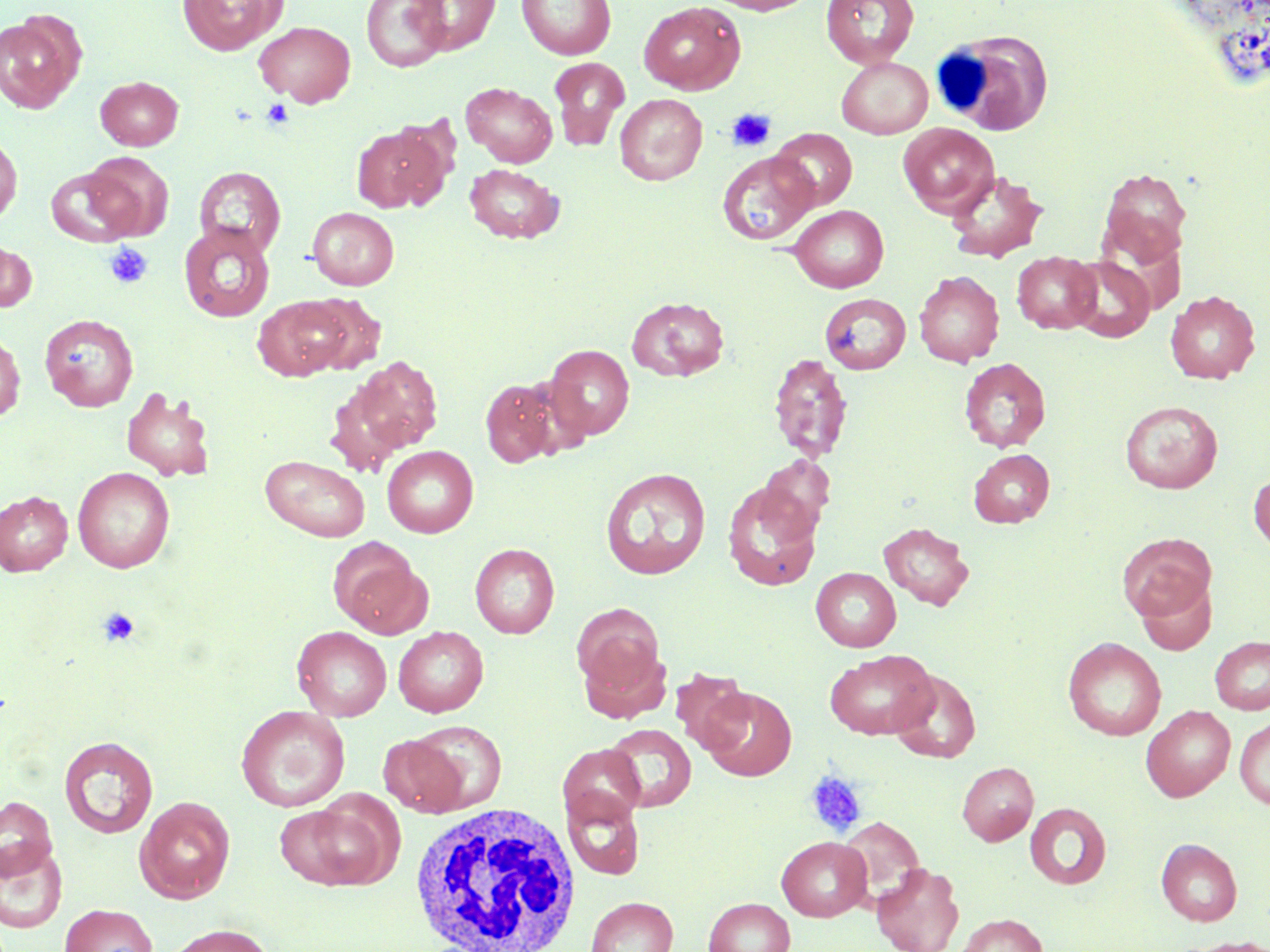 Approximate bounding boxes as [x1, y1, x2, y2] in pixels. Uninfected red blood cell locations: [177, 0, 286, 55], [361, 0, 451, 72], [408, 0, 501, 54], [517, 0, 616, 60], [705, 0, 817, 15], [821, 0, 919, 69], [639, 1, 745, 94], [0, 12, 84, 114], [254, 20, 356, 106], [549, 57, 630, 151], [836, 57, 933, 139], [96, 76, 183, 150], [461, 82, 557, 167], [615, 94, 707, 185], [898, 123, 999, 217], [351, 124, 448, 213], [770, 128, 857, 211], [0, 133, 22, 224], [718, 151, 817, 245], [84, 152, 174, 240], [464, 163, 564, 244], [194, 166, 286, 259], [46, 167, 139, 247], [1099, 168, 1191, 263], [945, 170, 1048, 263], [789, 205, 889, 293], [308, 207, 399, 290], [178, 222, 276, 322], [0, 238, 37, 312], [1012, 251, 1101, 333], [1066, 256, 1155, 341], [914, 270, 1005, 367], [1164, 290, 1260, 384], [303, 293, 387, 374], [822, 293, 912, 375], [252, 296, 350, 380], [627, 296, 729, 382], [40, 314, 138, 411], [0, 329, 26, 421], [545, 345, 635, 441], [768, 352, 853, 463], [344, 355, 444, 461], [959, 357, 1051, 452], [480, 378, 562, 467], [120, 386, 216, 483], [1120, 400, 1222, 494], [382, 446, 478, 537], [969, 449, 1055, 528], [757, 454, 835, 535], [261, 455, 370, 541], [72, 466, 175, 573], [601, 468, 711, 579], [1249, 470, 1270, 554], [722, 480, 822, 591], [0, 491, 72, 576], [878, 521, 974, 610], [1117, 532, 1217, 622], [329, 539, 431, 638], [470, 543, 559, 639], [811, 567, 900, 651], [1135, 576, 1218, 656], [572, 603, 665, 699], [292, 626, 392, 721], [393, 626, 488, 717], [1210, 636, 1270, 714], [1063, 637, 1166, 741], [577, 640, 672, 724], [826, 649, 937, 739], [670, 668, 753, 753], [891, 670, 981, 763], [699, 685, 797, 781], [236, 705, 350, 812], [1141, 705, 1235, 801], [1235, 717, 1270, 810], [405, 720, 508, 814], [604, 723, 697, 812], [58, 735, 158, 838], [380, 735, 468, 817], [558, 743, 646, 827], [957, 762, 1038, 845], [563, 792, 645, 880], [0, 795, 58, 882], [134, 796, 236, 903], [279, 796, 397, 891], [1024, 802, 1111, 890], [838, 816, 925, 904], [776, 836, 872, 921], [1156, 838, 1242, 926], [0, 841, 68, 934], [871, 861, 964, 952], [586, 896, 678, 952], [703, 897, 795, 952], [59, 903, 158, 952], [954, 913, 1048, 952], [163, 923, 277, 952], [1170, 937, 1270, 952]. White blood cell locations: [935, 28, 1056, 136], [408, 803, 582, 951]. Platelet locations: [261, 98, 294, 129], [726, 107, 776, 152], [103, 242, 153, 289], [97, 607, 139, 646], [804, 769, 867, 837]. Slide-level diagnosis: negative for blood parasites. Thin blood film. Captured at 1000x magnification. May-Grünwald-Giemsa-stained preparation. Optical microscopy. Image is 1270×952 pixels. One field of a larger specimen.